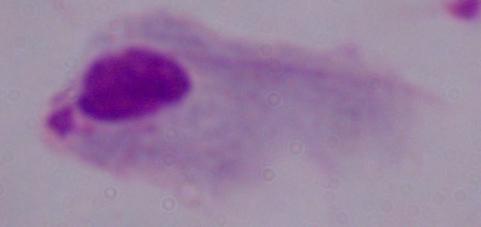 Photomicrograph. A trichomonad is seen. 1000x magnification.